State the blood parasite species.
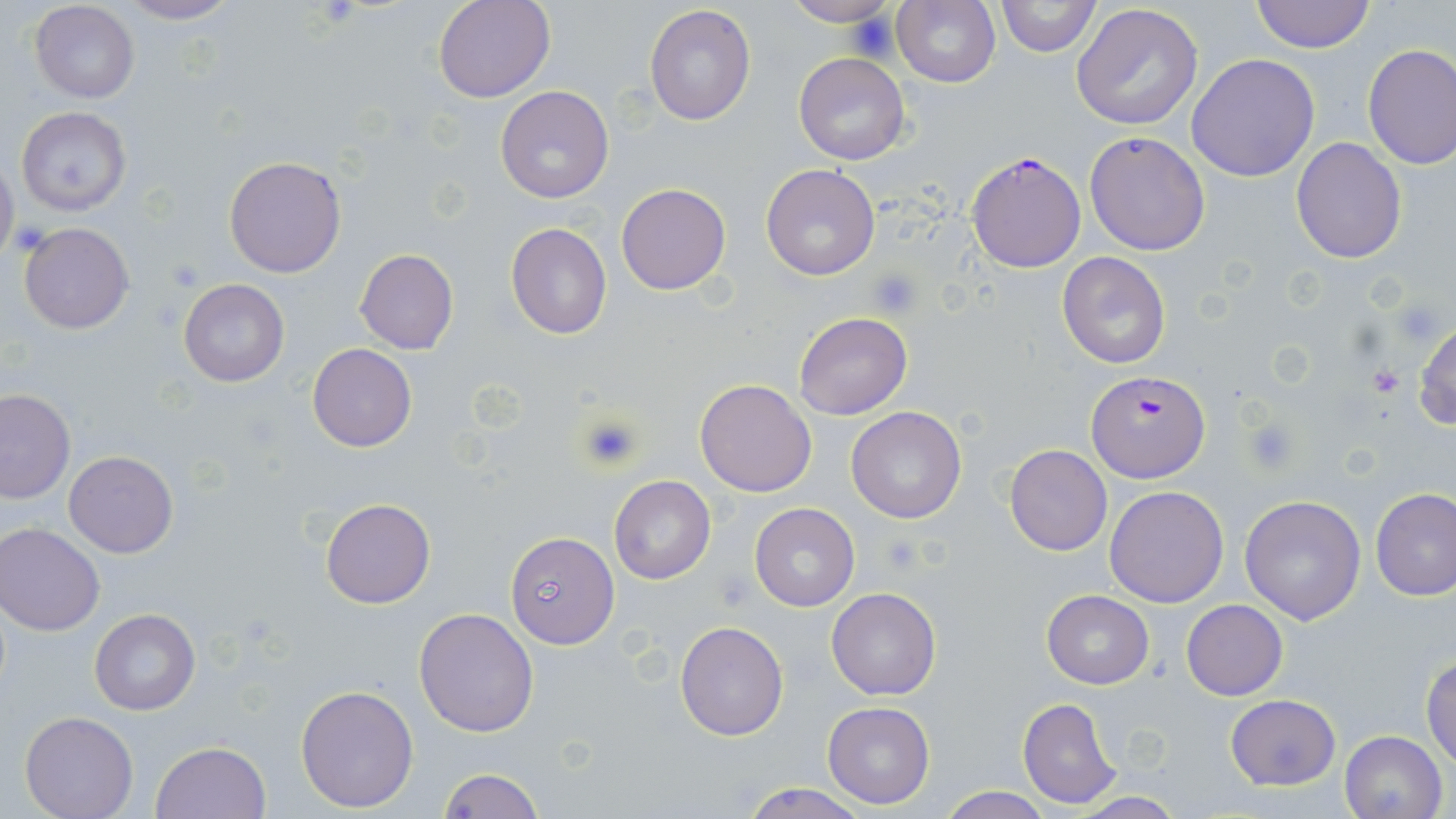
Plasmodium falciparum.

Summary:
  - Coordinate format: approximate bounding boxes as named x1/y1/x2/y2 corners in pixels
  - Uninfected red blood cell locations: (x1=113, y1=0, x2=243, y2=25), (x1=434, y1=0, x2=557, y2=104), (x1=781, y1=0, x2=898, y2=27), (x1=893, y1=0, x2=1001, y2=88), (x1=995, y1=0, x2=1101, y2=58), (x1=1249, y1=0, x2=1376, y2=52), (x1=29, y1=1, x2=140, y2=103), (x1=643, y1=5, x2=756, y2=126), (x1=1071, y1=5, x2=1204, y2=131), (x1=1361, y1=43, x2=1456, y2=170), (x1=794, y1=53, x2=909, y2=165), (x1=1187, y1=54, x2=1320, y2=181), (x1=495, y1=85, x2=614, y2=202), (x1=17, y1=105, x2=132, y2=217), (x1=1084, y1=131, x2=1210, y2=255), (x1=1292, y1=136, x2=1406, y2=262), (x1=0, y1=154, x2=20, y2=270), (x1=223, y1=155, x2=348, y2=278), (x1=760, y1=164, x2=882, y2=281), (x1=616, y1=183, x2=732, y2=296), (x1=19, y1=222, x2=134, y2=334), (x1=505, y1=223, x2=612, y2=339), (x1=355, y1=248, x2=458, y2=355), (x1=1057, y1=251, x2=1173, y2=369), (x1=178, y1=279, x2=289, y2=386), (x1=793, y1=312, x2=912, y2=421), (x1=1411, y1=314, x2=1455, y2=433), (x1=307, y1=343, x2=417, y2=452), (x1=695, y1=378, x2=817, y2=497), (x1=0, y1=389, x2=75, y2=504), (x1=845, y1=406, x2=967, y2=524), (x1=1005, y1=443, x2=1112, y2=556), (x1=64, y1=450, x2=179, y2=557), (x1=609, y1=475, x2=715, y2=585), (x1=1105, y1=486, x2=1229, y2=607), (x1=1370, y1=487, x2=1455, y2=601), (x1=1240, y1=495, x2=1366, y2=625), (x1=320, y1=498, x2=435, y2=608), (x1=749, y1=503, x2=859, y2=612), (x1=1, y1=524, x2=104, y2=635), (x1=505, y1=531, x2=619, y2=649), (x1=825, y1=587, x2=941, y2=700), (x1=1041, y1=590, x2=1154, y2=689), (x1=1182, y1=600, x2=1286, y2=700), (x1=413, y1=606, x2=541, y2=737), (x1=89, y1=608, x2=200, y2=714), (x1=675, y1=620, x2=789, y2=740), (x1=1421, y1=654, x2=1456, y2=767), (x1=295, y1=683, x2=420, y2=813), (x1=1224, y1=693, x2=1342, y2=791), (x1=1018, y1=697, x2=1121, y2=808), (x1=823, y1=700, x2=934, y2=808), (x1=19, y1=709, x2=139, y2=819), (x1=1339, y1=730, x2=1449, y2=819), (x1=153, y1=741, x2=271, y2=818), (x1=438, y1=767, x2=542, y2=819), (x1=738, y1=782, x2=873, y2=819), (x1=933, y1=787, x2=1053, y2=819), (x1=1072, y1=793, x2=1187, y2=818)
  - Platelet locations: (x1=848, y1=13, x2=902, y2=65), (x1=166, y1=257, x2=208, y2=292), (x1=870, y1=268, x2=922, y2=316), (x1=1368, y1=366, x2=1405, y2=396), (x1=578, y1=410, x2=646, y2=471), (x1=1241, y1=415, x2=1301, y2=473), (x1=714, y1=570, x2=754, y2=612)
  - Plasmodium falciparum-infected red blood cell locations: (x1=965, y1=150, x2=1087, y2=273), (x1=1087, y1=369, x2=1207, y2=482)
  - Field of view: one of a larger specimen
  - Stain: May-Grünwald-Giemsa
  - Preparation: thin blood film
  - Image size: 1456×819 pixels
  - Magnification: 1000x
  - Modality: light microscopy